Name the parasite shown.
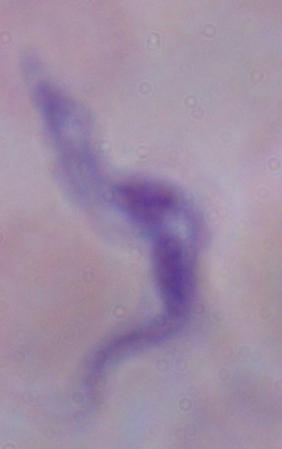
A trypanosome.

Summary:
  - Magnification: 1000x
  - Modality: photomicrograph